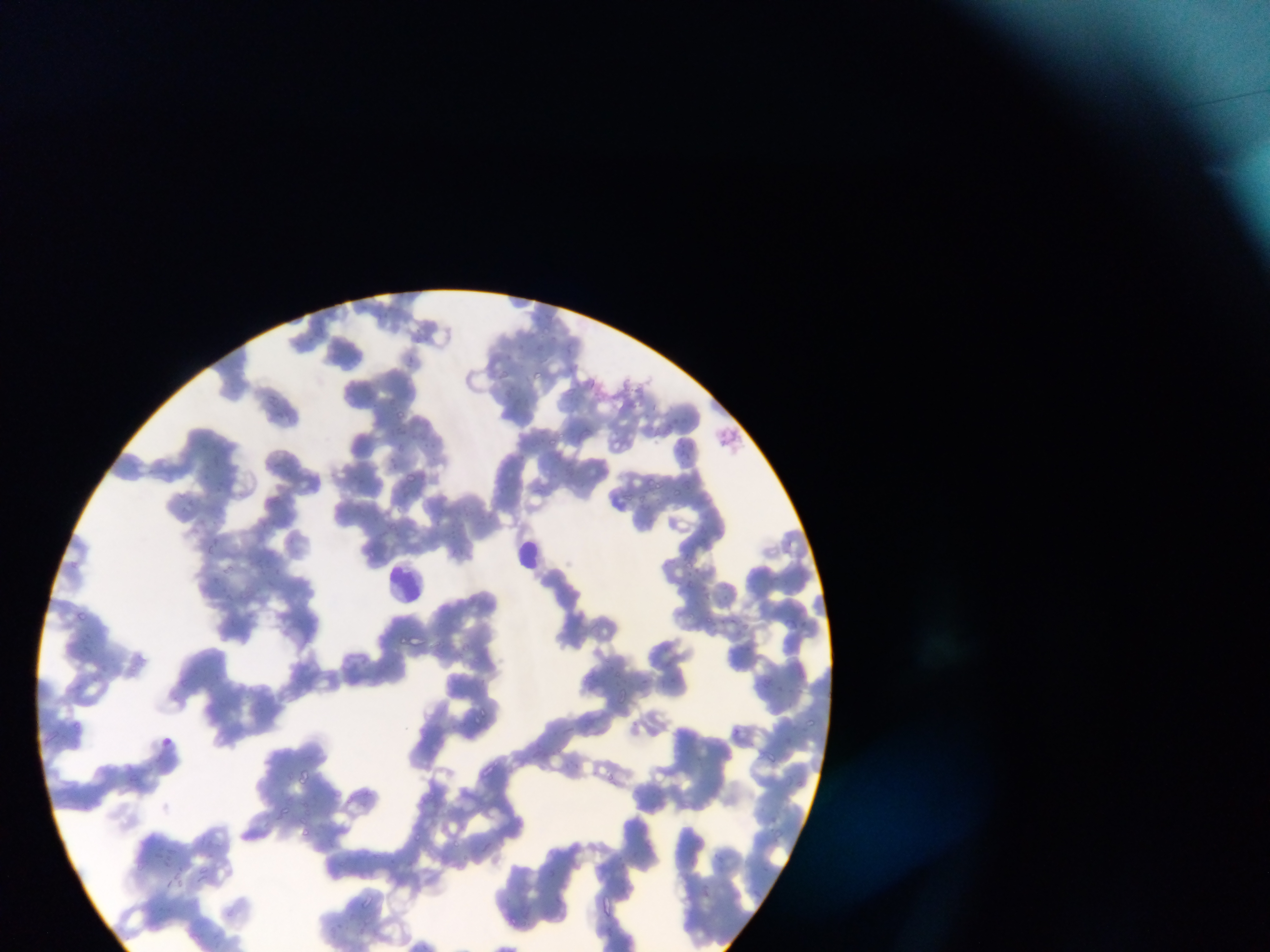
Approximate bounding boxes as [left, top, right, bottom] in pixels.
Summary:
  - Leukocyte locations: [513, 538, 547, 568], [387, 562, 427, 601]
  - Malaria parasite locations: [413, 327, 428, 339], [519, 339, 532, 349], [506, 350, 518, 360], [405, 355, 425, 370], [224, 366, 236, 376], [534, 368, 545, 381], [497, 369, 508, 380], [581, 374, 603, 388], [350, 388, 361, 399], [267, 396, 281, 411], [398, 411, 408, 419], [667, 415, 685, 425], [398, 428, 411, 434], [551, 437, 556, 447], [425, 439, 446, 456], [397, 444, 407, 455], [681, 445, 691, 461], [212, 451, 221, 459], [281, 453, 301, 465], [388, 456, 399, 469], [203, 466, 214, 478], [215, 471, 231, 490], [405, 472, 419, 485], [355, 473, 362, 487], [645, 473, 659, 484], [674, 485, 683, 495], [640, 489, 654, 502], [622, 491, 637, 503], [188, 496, 204, 507], [462, 500, 479, 519], [482, 509, 502, 522], [449, 522, 460, 533], [214, 537, 222, 544], [207, 543, 216, 551], [683, 560, 702, 571], [274, 563, 290, 577], [228, 564, 236, 572], [213, 573, 226, 584], [720, 577, 733, 590], [686, 581, 698, 595], [720, 593, 730, 604], [706, 612, 717, 625], [727, 613, 738, 627], [789, 616, 805, 633], [744, 618, 756, 634], [395, 634, 412, 645], [668, 673, 678, 687], [637, 674, 651, 688], [767, 679, 777, 689], [796, 680, 814, 702], [618, 689, 632, 708], [478, 703, 488, 714], [474, 714, 482, 728], [805, 717, 814, 727], [732, 729, 742, 742], [765, 751, 782, 768], [478, 762, 497, 781], [295, 769, 314, 785], [607, 771, 616, 781], [277, 801, 288, 812], [297, 807, 307, 823], [771, 824, 784, 840], [298, 827, 308, 835], [415, 829, 421, 837], [451, 838, 467, 852], [162, 852, 177, 867], [361, 891, 374, 906], [509, 915, 520, 925] | approximate [x, y] pixel centers of objects too small to bound: [545, 328]
  - Image size: 1270×952 pixels
  - Field of view: single
  - Preparation: thin blood smear
  - Capture: mobile-phone photograph through a microscope
  - Country: Ghana